Comment on the morphology of the erythrocytes.
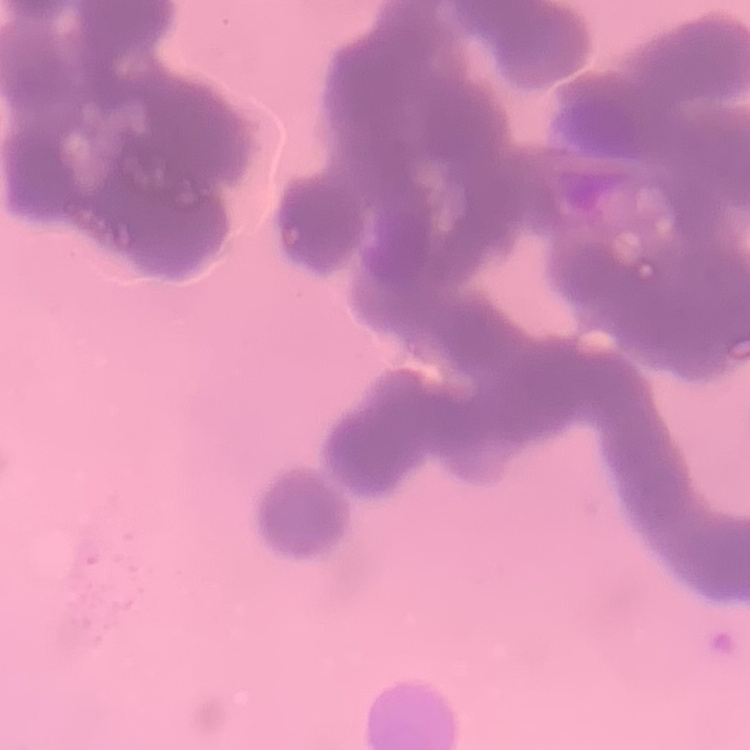
They show rouleaux formation.

{
  "stain": "Field's or Giemsa",
  "preparation": "thin peripheral smear",
  "image_type": "square crop of a larger photomicrograph"
}